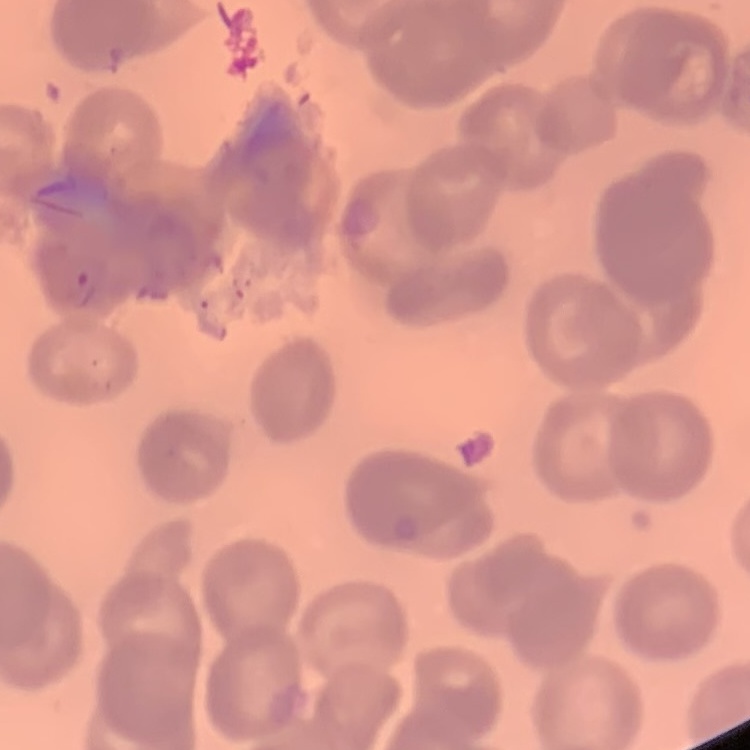 The red blood cells exhibit no rouleaux formation. Field's or Giemsa stain. Square crop of a larger photomicrograph. Thin blood smear.